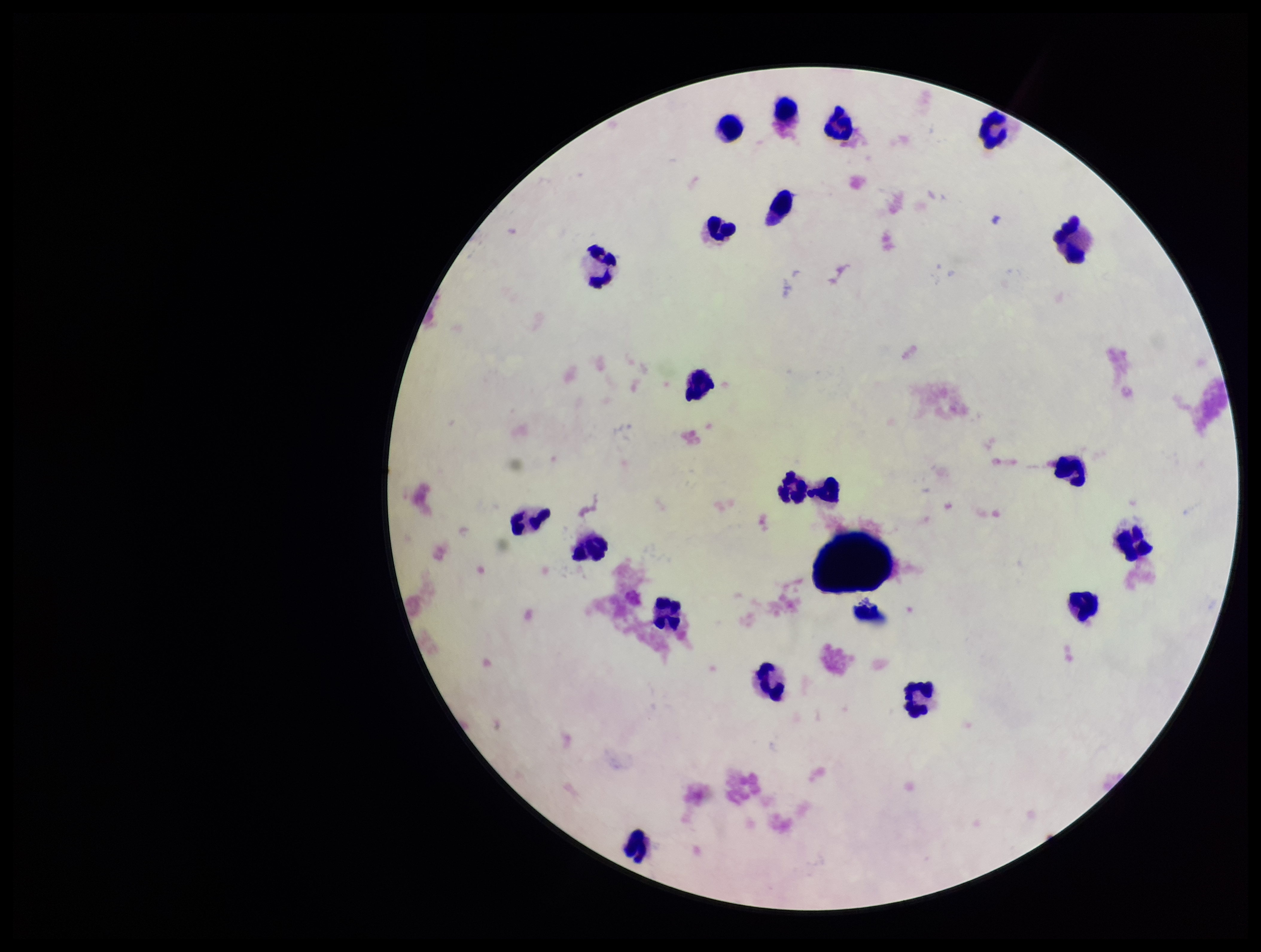

{
  "plasmodium_parasites": "none detected",
  "field_of_view": "one from this slide",
  "capture": "smartphone photograph through the microscope eyepiece",
  "parasite_count": 0,
  "patient_malaria_status": "negative",
  "preparation": "thick smear",
  "stain": "Giemsa",
  "image_size": "1261×952 pixels",
  "leukocyte_count": 19
}